Outline each blood parasite and name the species.
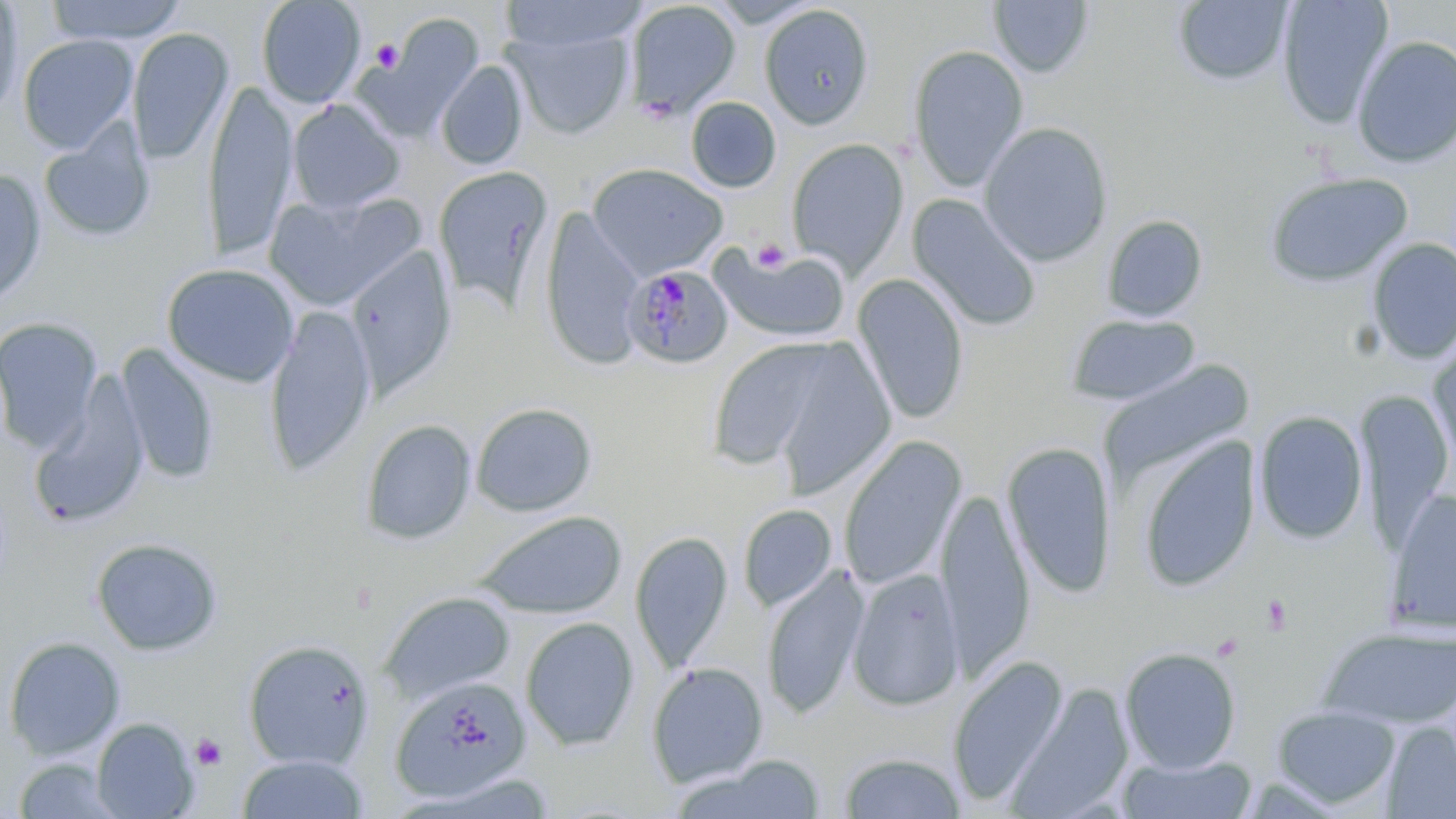

Approximate bounding boxes as (x1,y1)-(x2,y2) corner pairs in pixels.
Plasmodium malariae-infected red blood cells: (622,265)-(733,369).
No Plasmodium falciparum, Plasmodium ovale, Plasmodium vivax, Babesia divergens, or Trypanosoma brucei observed.

Summary:
  - Uninfected red blood cell locations: (45,0)-(188,45), (255,0)-(366,108), (707,0)-(823,27), (1276,0)-(1394,129), (0,1)-(25,122), (499,1)-(649,54), (625,1)-(741,118), (988,1)-(1094,78), (1172,1)-(1294,86), (760,5)-(874,130), (365,15)-(485,139), (506,23)-(635,139), (127,28)-(233,166), (17,34)-(137,153), (1351,35)-(1456,168), (908,45)-(1029,191), (436,60)-(529,170), (204,79)-(297,263), (687,97)-(781,193), (286,99)-(406,214), (38,117)-(156,244), (978,121)-(1113,266), (787,139)-(908,277), (587,163)-(727,278), (433,166)-(555,313), (0,168)-(46,311), (1263,171)-(1414,290), (264,190)-(424,311), (907,194)-(1042,332), (541,208)-(645,372), (1101,214)-(1208,322), (1366,238)-(1456,364), (346,243)-(456,403), (712,245)-(851,342), (161,263)-(299,387), (852,274)-(970,426), (265,303)-(376,478), (1065,313)-(1202,407), (0,316)-(102,454), (1428,335)-(1456,478), (705,339)-(835,471), (763,341)-(896,500), (115,343)-(220,486), (1100,362)-(1254,484), (31,373)-(152,529), (1356,390)-(1453,550), (471,402)-(597,517), (1254,410)-(1368,544), (361,419)-(477,544), (838,435)-(966,592), (1135,437)-(1261,592), (1001,442)-(1117,599), (1385,488)-(1456,637), (936,489)-(1036,679), (738,503)-(838,613), (469,510)-(628,620), (630,530)-(733,672), (91,537)-(224,657), (762,567)-(867,719), (848,569)-(964,712), (379,591)-(517,705), (520,616)-(639,751), (1317,625)-(1456,731), (3,636)-(126,760), (242,639)-(374,770), (1119,646)-(1241,774), (946,653)-(1069,808), (647,661)-(768,789), (391,676)-(532,802), (1005,683)-(1133,818), (1271,705)-(1400,809), (91,717)-(198,818), (1380,722)-(1456,818), (836,752)-(967,818), (235,754)-(370,818), (1117,754)-(1259,819), (676,755)-(833,819), (13,758)-(125,818)
  - Platelet locations: (370,39)-(403,73), (751,238)-(792,274), (1259,593)-(1295,637), (190,733)-(228,770)
  - Slide-level diagnosis: Plasmodium malariae
  - Magnification: 1000x
  - Field of view: one of a larger specimen
  - Image size: 1456×819 pixels
  - Preparation: thin blood smear
  - Stain: May-Grünwald-Giemsa
  - Modality: light microscopy